Classify this cell by malaria status.
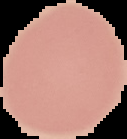
It is uninfected.

The area outside the segmented cell region is set to black. From a thin blood smear. Image is 127×139 pixels.